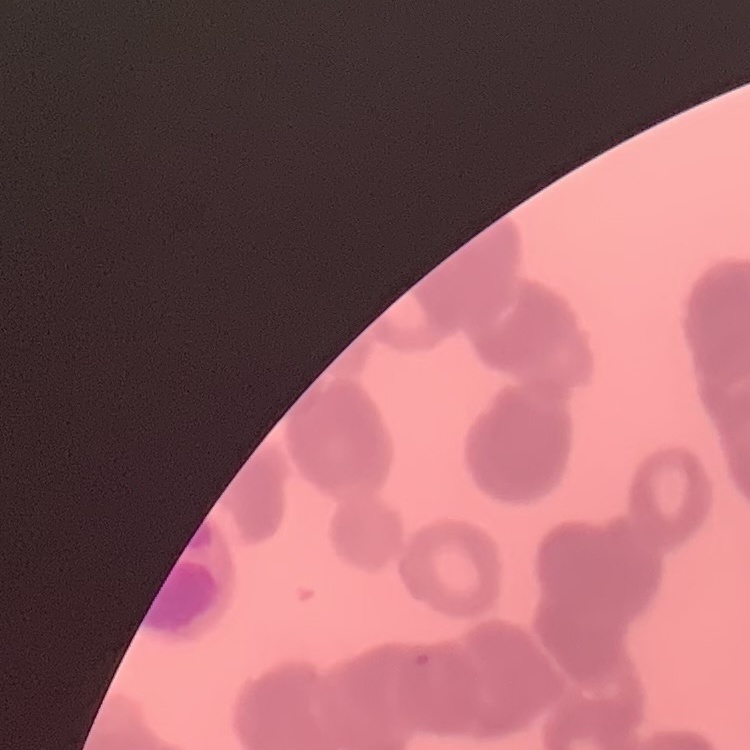 The erythrocytes show rouleaux formation. Field's or Giemsa stain. Thin blood smear. One tile cut from a larger photomicrograph.